Report the malaria status of this cell.
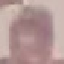
It is uninfected.

Thin blood film. Giemsa stain. Automatically extracted cell patch, resized to 64 × 64 pixels. Acquired by smartphone through the microscope eyepiece.